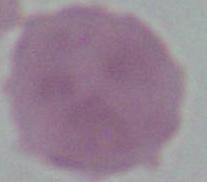
identification = erythrocyte
modality = micrograph
magnification = 1000x